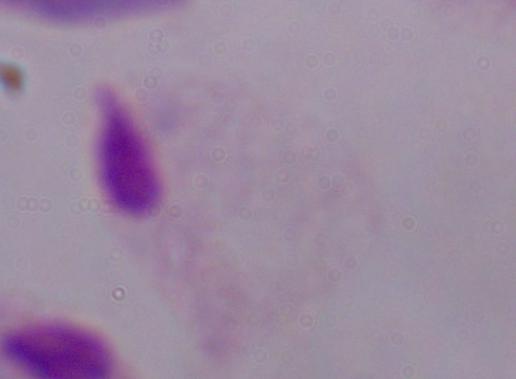
modality: photomicrograph
identification: trichomonad
magnification: 1000x